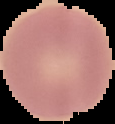
Summary:
  - Image type: segmented cell region with the area outside set to black
  - Preparation: thin blood film
  - Result: no Plasmodium parasites seen
  - Image size: 115×124 pixels